Identify the parasite.
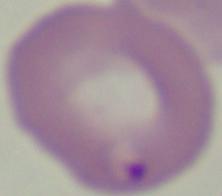

This is Babesia.

magnification = 1000x
modality = micrograph